Classify this cell by malaria status.
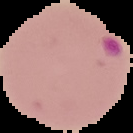
It is parasitized.

Summary:
  - Image size: 133×133 pixels
  - Preparation: thin blood film
  - Image type: cell region segmented out of the field of view; surrounding area masked to black